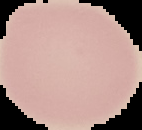

Cell region segmented out of the field of view; the surrounding area is masked to black. Result: negative for malaria parasites. From a thin blood smear. Image is 142×130 pixels.